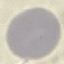

Summary:
  - Result: no malaria parasites detected
  - Capture: smartphone through the microscope eyepiece
  - Stain: Giemsa
  - Image type: cell patch, automatically extracted from a larger field of view and resized to 64 × 64 pixels
  - Preparation: thin smear